Classify this cell by malaria status.
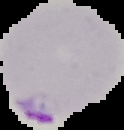

Parasitized.

image_size: 124×130 pixels
preparation: thin blood film
image_type: cell region segmented out of the field of view; surrounding area masked to black